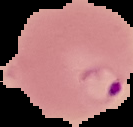 Segmented cell region on a black background. Image is 133×127 pixels. From a thin blood smear. Malaria status: parasitized.